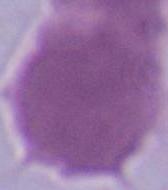 Captured at 1000x magnification. An erythrocyte is seen. Photomicrograph.